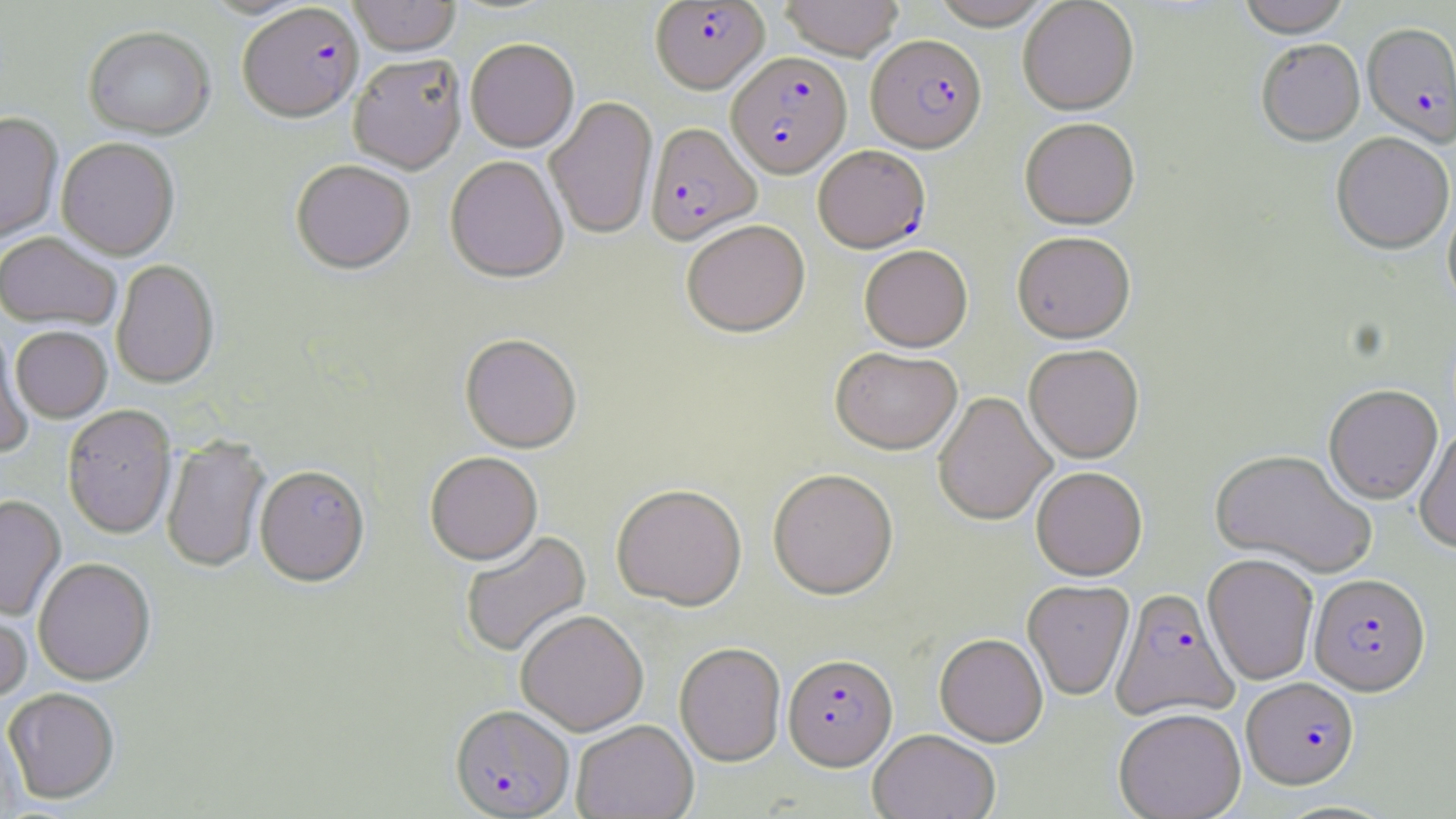
slide-level diagnosis = Plasmodium falciparum
modality = light microscopy
uninfected red blood cell locations = approximate bounding boxes as named x1/y1/x2/y2 corners in pixels: (x1=348, y1=0, x2=461, y2=57), (x1=780, y1=0, x2=904, y2=60), (x1=930, y1=0, x2=1055, y2=29), (x1=1018, y1=0, x2=1139, y2=116), (x1=1237, y1=0, x2=1351, y2=39), (x1=83, y1=26, x2=215, y2=141), (x1=466, y1=39, x2=579, y2=153), (x1=1257, y1=41, x2=1365, y2=148), (x1=348, y1=54, x2=467, y2=175), (x1=545, y1=96, x2=657, y2=240), (x1=0, y1=112, x2=64, y2=244), (x1=1020, y1=119, x2=1140, y2=231), (x1=1331, y1=134, x2=1455, y2=257), (x1=56, y1=139, x2=180, y2=260), (x1=445, y1=156, x2=568, y2=283), (x1=291, y1=161, x2=416, y2=275), (x1=1442, y1=195, x2=1456, y2=316), (x1=682, y1=221, x2=810, y2=338), (x1=0, y1=233, x2=121, y2=331), (x1=1012, y1=233, x2=1136, y2=345), (x1=859, y1=245, x2=973, y2=353), (x1=112, y1=260, x2=219, y2=389), (x1=11, y1=327, x2=112, y2=422), (x1=0, y1=329, x2=34, y2=456), (x1=460, y1=335, x2=582, y2=453), (x1=1024, y1=345, x2=1144, y2=464), (x1=831, y1=348, x2=962, y2=455), (x1=1323, y1=386, x2=1443, y2=506), (x1=933, y1=392, x2=1056, y2=527), (x1=62, y1=405, x2=177, y2=540), (x1=1415, y1=427, x2=1456, y2=554), (x1=161, y1=436, x2=270, y2=573), (x1=1210, y1=450, x2=1377, y2=579), (x1=425, y1=452, x2=543, y2=565), (x1=255, y1=466, x2=370, y2=587), (x1=1031, y1=467, x2=1147, y2=581), (x1=768, y1=469, x2=899, y2=601), (x1=611, y1=485, x2=747, y2=612), (x1=0, y1=495, x2=66, y2=621), (x1=460, y1=531, x2=592, y2=658), (x1=1203, y1=555, x2=1318, y2=686), (x1=33, y1=558, x2=156, y2=687), (x1=1023, y1=581, x2=1134, y2=701), (x1=0, y1=597, x2=32, y2=704), (x1=515, y1=610, x2=649, y2=736), (x1=934, y1=634, x2=1048, y2=747), (x1=674, y1=643, x2=786, y2=767), (x1=3, y1=689, x2=120, y2=805), (x1=1113, y1=710, x2=1247, y2=819), (x1=0, y1=720, x2=24, y2=818), (x1=571, y1=720, x2=698, y2=819), (x1=868, y1=731, x2=1000, y2=819)
image size = 1456×819 pixels
stain = May-Grünwald-Giemsa
field of view = single
Plasmodium falciparum-infected red blood cell locations = approximate bounding boxes as named x1/y1/x2/y2 corners in pixels: (x1=650, y1=1, x2=769, y2=93), (x1=238, y1=4, x2=364, y2=124), (x1=1362, y1=24, x2=1455, y2=149), (x1=866, y1=34, x2=987, y2=152), (x1=726, y1=52, x2=852, y2=178), (x1=645, y1=122, x2=762, y2=246), (x1=813, y1=146, x2=930, y2=253), (x1=1309, y1=574, x2=1431, y2=697), (x1=1111, y1=587, x2=1239, y2=721), (x1=783, y1=655, x2=898, y2=771), (x1=1241, y1=678, x2=1360, y2=790), (x1=450, y1=706, x2=574, y2=818)
magnification = 1000x
preparation = thin blood film